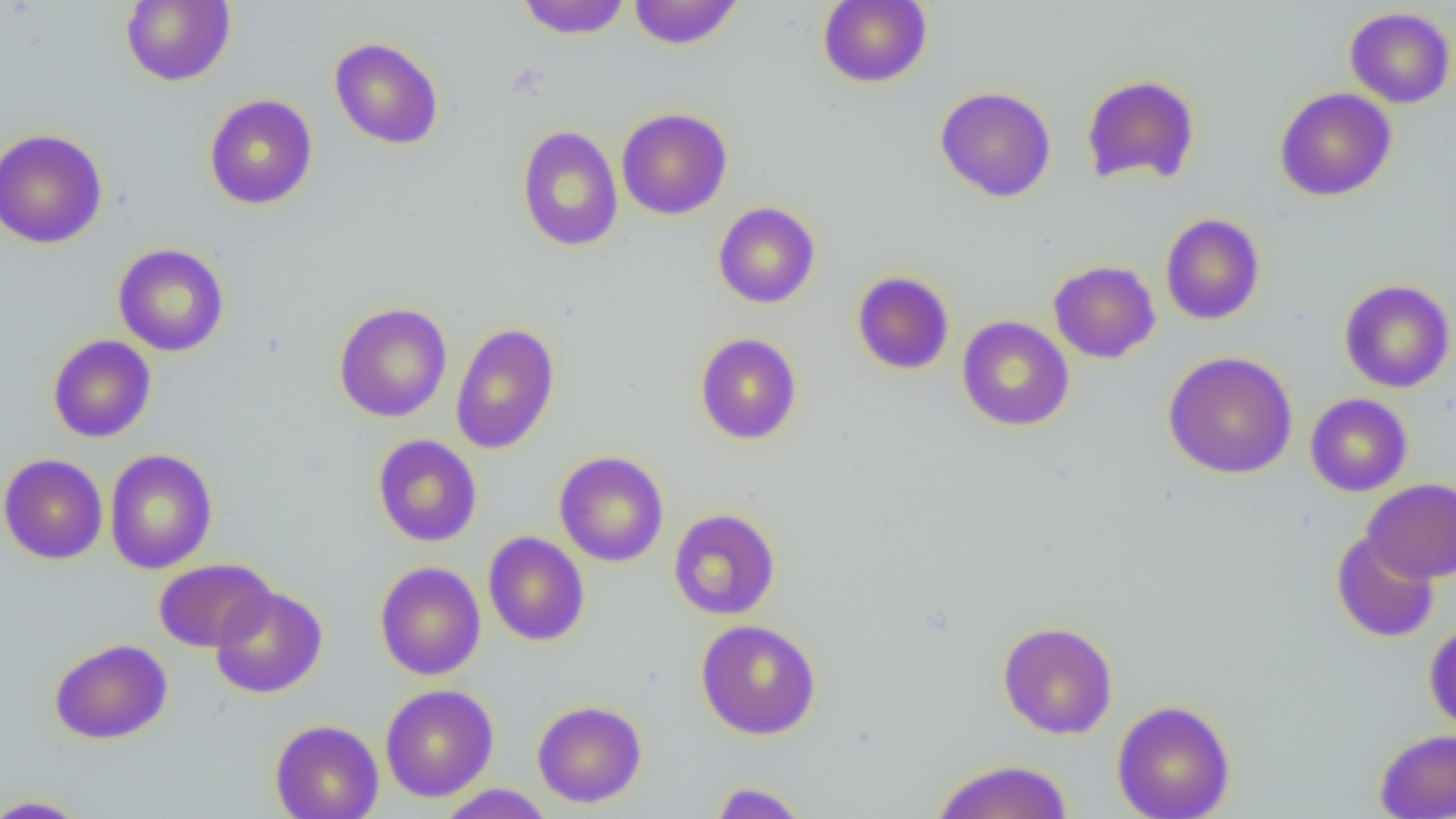

Approximate bounding boxes as (x1,y1)-(x2,y2) corner pairs in pixels. Uninfected red blood cell locations: (121,0)-(235,86), (517,0)-(630,39), (627,0)-(743,50), (818,0)-(932,88), (1344,7)-(1455,108), (330,37)-(444,150), (1081,74)-(1201,187), (935,86)-(1057,203), (1275,87)-(1397,201), (204,94)-(317,210), (616,107)-(733,220), (517,125)-(623,252), (0,128)-(108,249), (713,201)-(821,309), (1160,213)-(1266,325), (113,244)-(229,356), (1049,260)-(1160,364), (852,271)-(955,375), (1339,279)-(1455,393), (334,302)-(452,423), (957,315)-(1074,431), (450,322)-(560,454), (695,332)-(802,445), (47,335)-(156,442), (1163,351)-(1298,479), (1305,393)-(1413,497), (372,434)-(482,547), (104,449)-(217,574), (554,451)-(669,567), (0,453)-(108,564), (1362,479)-(1456,583), (668,508)-(781,620), (1331,530)-(1440,642), (483,531)-(590,646), (153,558)-(276,652), (375,561)-(486,680), (209,585)-(328,699), (696,619)-(822,740), (997,621)-(1118,740), (1424,622)-(1456,733), (49,638)-(173,744), (380,684)-(498,802), (1112,699)-(1236,819), (532,700)-(647,808), (269,719)-(384,819), (1374,729)-(1456,818), (930,759)-(1074,818), (709,781)-(809,818), (436,784)-(555,818), (0,795)-(91,818). Slide-level diagnosis: negative for blood parasites. Light microscopy. Captured at 1000x magnification. Image is 1456×819 pixels. Thin blood film. Single field of view.